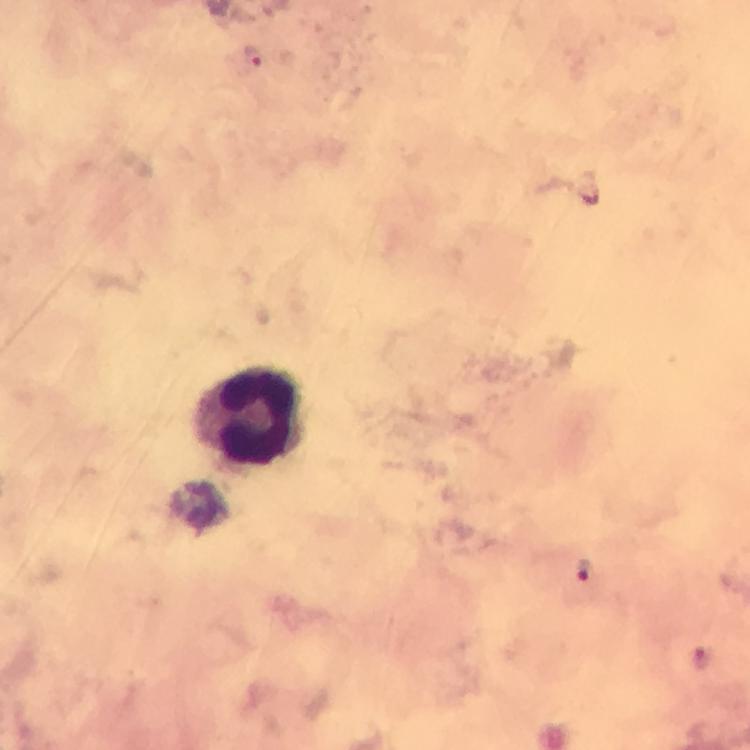
Approximate centers as {x, y} in pixels.
Summary:
  - Malaria parasite locations: {253, 56}, {584, 568}, {702, 656}
  - Leukocyte locations: {247, 414}
  - Image size: 750×750 pixels
  - Context: from a malaria diagnostic workup
  - Magnification: 100x
  - Stain: Giemsa
  - Preparation: thick blood smear
  - Capture: smartphone photograph through a microscope
  - Immersion oil: applied
  - Cropped from: one field of view